State which parasite is depicted.
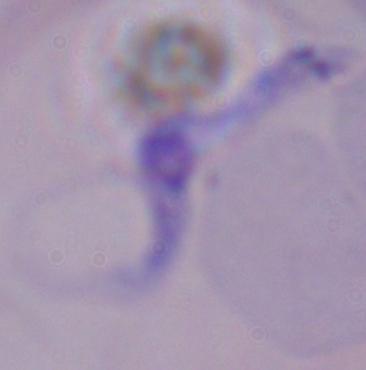
A trypanosome.

modality = photomicrograph
magnification = 1000x